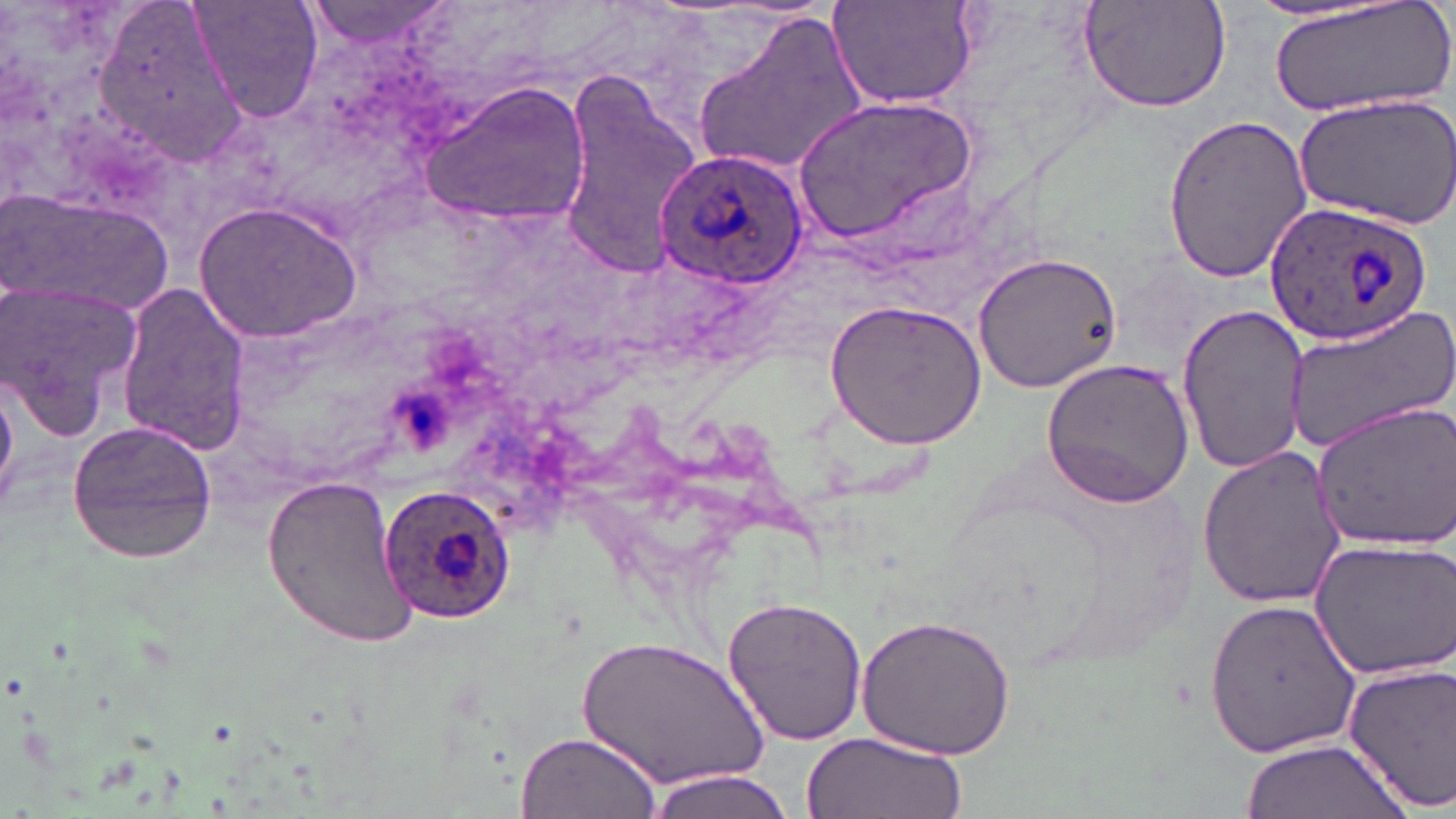
Summary:
  - Coordinate format: approximate bounding boxes as [x1, y1, x2, y2] in pixels
  - Uninfected red blood cell locations: [95, 0, 245, 164], [186, 0, 325, 124], [829, 0, 983, 112], [1077, 0, 1234, 113], [1267, 0, 1456, 118], [303, 2, 456, 54], [691, 9, 868, 181], [556, 71, 702, 272], [419, 80, 591, 231], [1294, 93, 1456, 228], [795, 96, 979, 242], [1158, 114, 1315, 281], [0, 187, 169, 324], [194, 201, 362, 345], [972, 251, 1123, 394], [2, 278, 143, 440], [116, 281, 254, 453], [825, 299, 986, 449], [1283, 303, 1456, 453], [1177, 305, 1312, 475], [1041, 358, 1198, 508], [0, 375, 16, 509], [1309, 401, 1455, 554], [65, 420, 218, 565], [1195, 445, 1349, 609], [261, 470, 417, 650], [1306, 534, 1455, 683], [720, 594, 871, 748], [1205, 595, 1362, 761], [855, 616, 1018, 760], [575, 637, 769, 792], [1343, 659, 1456, 810], [517, 730, 660, 818], [799, 730, 965, 819], [1240, 739, 1407, 818], [644, 767, 800, 819]
  - Plasmodium ovale-infected red blood cell locations: [654, 148, 808, 288], [1266, 202, 1432, 346], [376, 481, 519, 626]
  - Slide-level diagnosis: Plasmodium ovale
  - Stain: May-Grünwald-Giemsa
  - Modality: optical microscopy
  - Preparation: thin blood smear
  - Magnification: 1000x
  - Field of view: one of a larger specimen
  - Image size: 1456×819 pixels